Name the parasite shown.
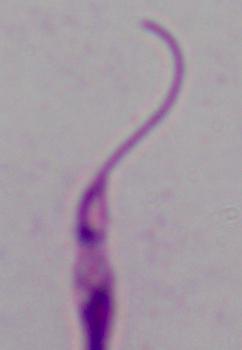
Leishmania.

Summary:
  - Magnification: 1000x
  - Modality: micrograph